Name the cell type shown.
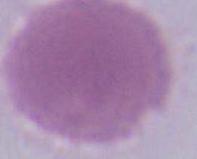
An erythrocyte.

magnification = 1000x
modality = micrograph